Identify the parasite.
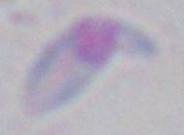
Toxoplasma gondii.

modality: micrograph
magnification: 1000x